Locate every Plasmodium falciparum-infected red blood cell.
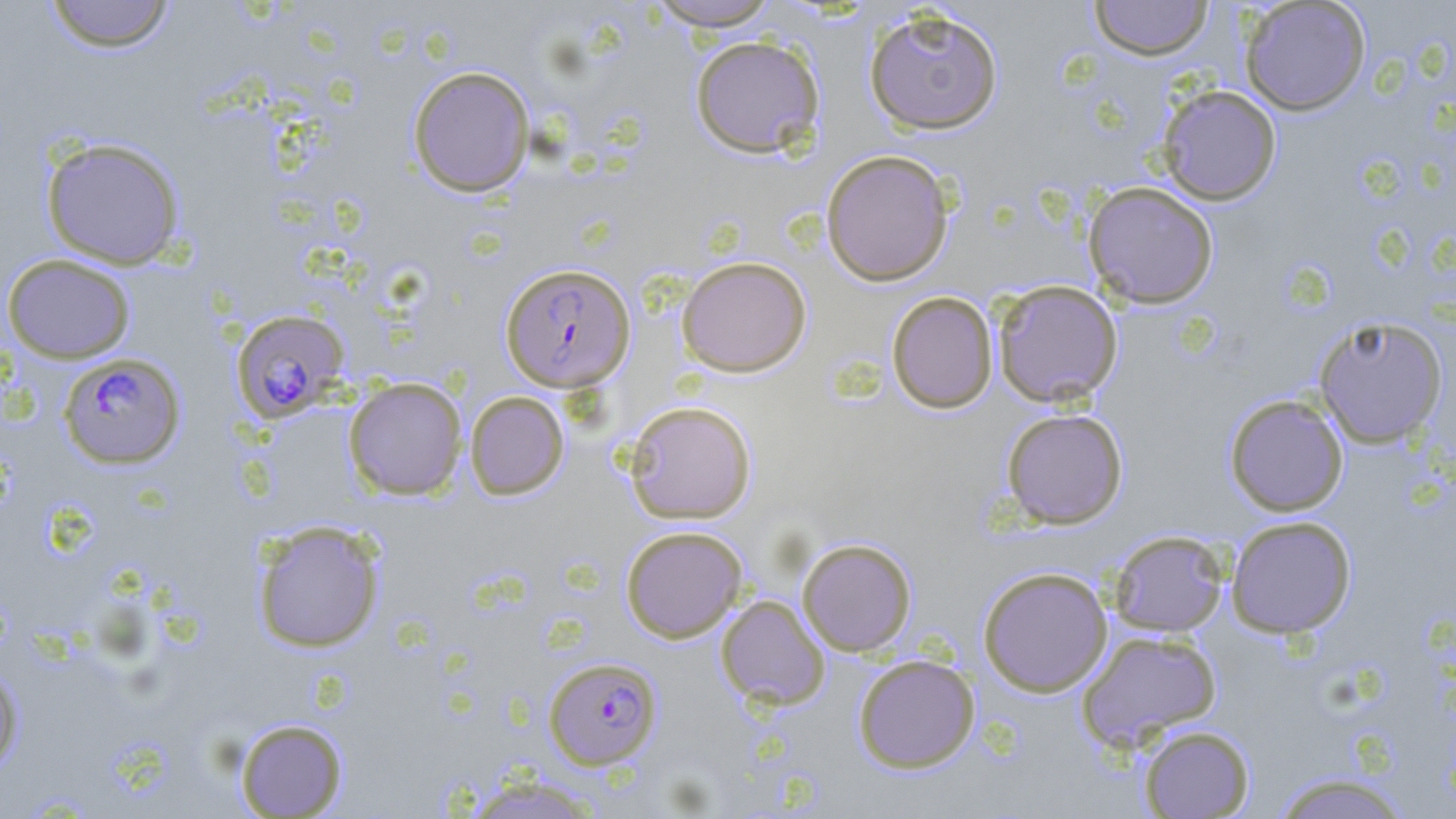

Approximate bounding boxes as named x1/y1/x2/y2 corners in pixels.
Plasmodium falciparum-infected red blood cells: (x1=500, y1=262, x2=635, y2=393), (x1=231, y1=308, x2=350, y2=423), (x1=58, y1=352, x2=186, y2=469), (x1=543, y1=657, x2=662, y2=769).

Uninfected red blood cell locations: (x1=44, y1=0, x2=175, y2=53), (x1=644, y1=0, x2=784, y2=31), (x1=1089, y1=0, x2=1215, y2=61), (x1=1240, y1=1, x2=1370, y2=116), (x1=864, y1=7, x2=1004, y2=135), (x1=689, y1=35, x2=825, y2=158), (x1=408, y1=65, x2=535, y2=197), (x1=1157, y1=85, x2=1282, y2=205), (x1=40, y1=136, x2=187, y2=270), (x1=821, y1=149, x2=955, y2=286), (x1=1083, y1=181, x2=1219, y2=309), (x1=2, y1=253, x2=136, y2=363), (x1=676, y1=256, x2=812, y2=377), (x1=992, y1=279, x2=1123, y2=407), (x1=887, y1=291, x2=998, y2=414), (x1=1313, y1=315, x2=1448, y2=448), (x1=343, y1=376, x2=468, y2=500), (x1=464, y1=391, x2=569, y2=500), (x1=1224, y1=394, x2=1349, y2=517), (x1=624, y1=400, x2=757, y2=524), (x1=1000, y1=407, x2=1129, y2=529), (x1=1225, y1=515, x2=1357, y2=638), (x1=252, y1=520, x2=385, y2=653), (x1=620, y1=525, x2=748, y2=643), (x1=1108, y1=530, x2=1229, y2=636), (x1=797, y1=538, x2=917, y2=656), (x1=977, y1=566, x2=1113, y2=697), (x1=716, y1=595, x2=830, y2=709), (x1=1076, y1=628, x2=1222, y2=750), (x1=852, y1=653, x2=980, y2=773), (x1=0, y1=667, x2=24, y2=774), (x1=234, y1=718, x2=348, y2=817), (x1=1137, y1=724, x2=1254, y2=818), (x1=1268, y1=771, x2=1414, y2=818), (x1=458, y1=774, x2=607, y2=818). Slide-level diagnosis: Plasmodium falciparum. One field of a larger specimen. Image is 1456×819 pixels. Light microscopy. Captured at 1000x magnification. Thin blood film. May-Grünwald-Giemsa stain.